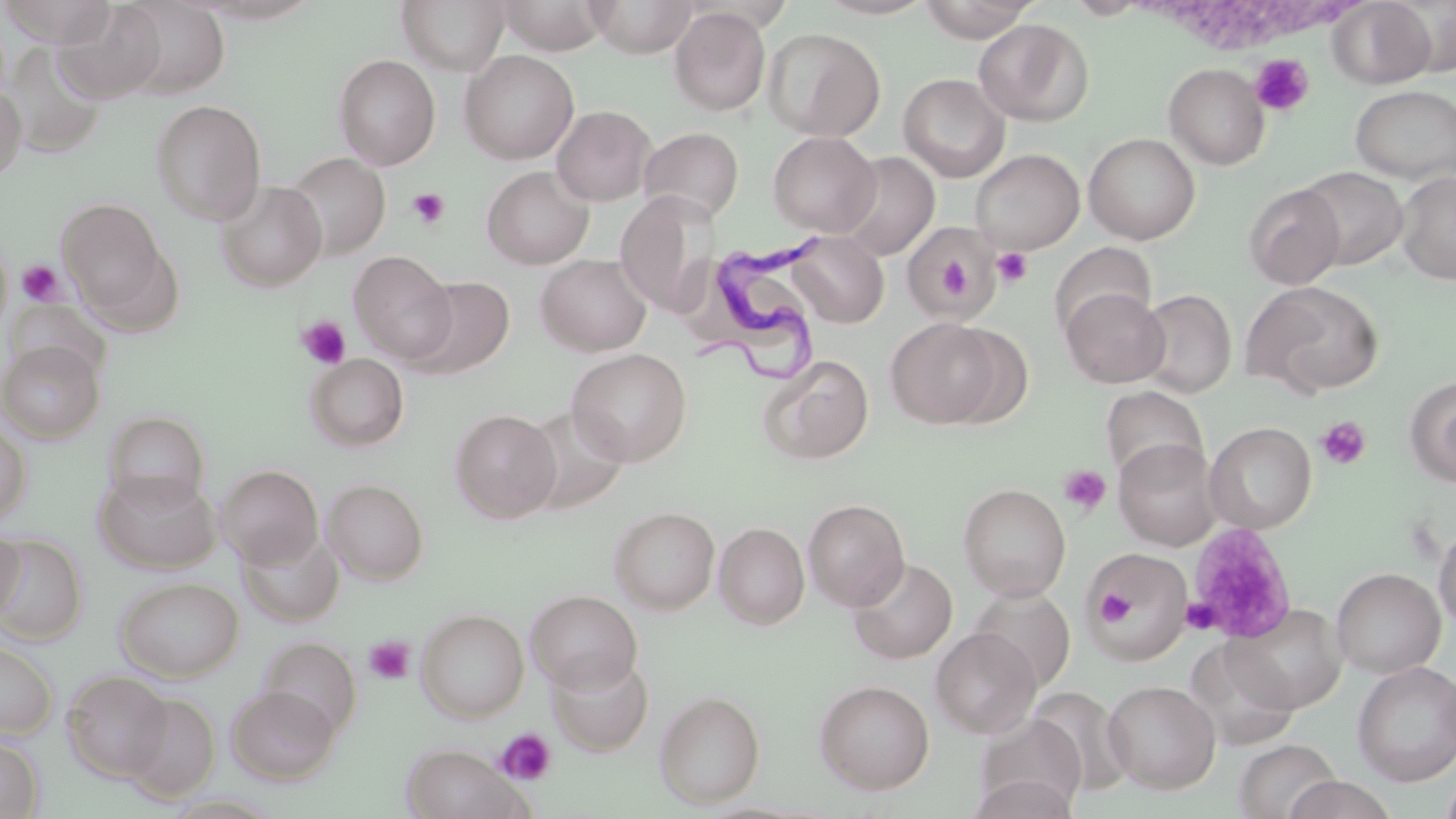 Approximate bounding boxes as [x1, y1, x2, y2] in pixels. Platelet locations: [1250, 53, 1315, 117], [407, 187, 450, 229], [992, 246, 1034, 288], [16, 260, 65, 306], [297, 315, 351, 370], [1316, 417, 1372, 470], [1058, 465, 1111, 516], [1186, 522, 1296, 641], [1097, 585, 1137, 630], [1181, 597, 1221, 634], [364, 636, 415, 686], [495, 727, 557, 785]. Trypanosoma brucei locations: [702, 231, 827, 380]. Uninfected red blood cell locations: [1, 0, 116, 46], [117, 0, 229, 97], [397, 0, 510, 75], [494, 0, 610, 54], [586, 0, 700, 57], [814, 0, 937, 19], [916, 0, 1040, 42], [1328, 0, 1435, 88], [54, 2, 167, 103], [669, 7, 770, 116], [973, 18, 1094, 126], [763, 27, 885, 141], [5, 44, 106, 159], [459, 50, 579, 164], [333, 54, 441, 170], [1164, 63, 1270, 169], [898, 73, 1010, 182], [0, 82, 27, 183], [1350, 84, 1456, 183], [150, 99, 266, 224], [551, 105, 656, 206], [637, 127, 744, 224], [768, 131, 881, 236], [1083, 133, 1200, 244], [970, 148, 1084, 253], [836, 151, 940, 260], [284, 152, 390, 258], [482, 165, 594, 269], [1297, 167, 1407, 269], [1396, 171, 1456, 284], [216, 181, 327, 291], [1244, 182, 1345, 289], [621, 196, 728, 320], [57, 198, 168, 313], [900, 222, 1002, 322], [787, 231, 889, 328], [1049, 242, 1157, 339], [349, 251, 457, 364], [536, 254, 652, 356], [406, 276, 514, 380], [1243, 279, 1385, 398], [1062, 288, 1169, 388], [1137, 289, 1237, 397], [6, 298, 109, 380], [885, 318, 1003, 428], [0, 341, 104, 442], [567, 348, 693, 467], [305, 353, 410, 452], [759, 353, 874, 464], [1406, 376, 1456, 488], [1101, 386, 1207, 485], [449, 408, 561, 524], [103, 410, 210, 509], [0, 419, 31, 524], [1204, 422, 1317, 533], [1114, 437, 1221, 549], [216, 464, 324, 567], [94, 469, 221, 574], [322, 478, 429, 584], [958, 482, 1071, 600], [803, 499, 909, 610], [609, 507, 720, 614], [1434, 518, 1456, 633], [714, 522, 809, 629], [0, 526, 25, 623], [238, 528, 343, 627], [0, 535, 88, 644], [1088, 548, 1192, 664], [847, 557, 957, 664], [1331, 567, 1445, 677], [114, 576, 244, 682], [969, 586, 1076, 690], [525, 589, 643, 693], [1225, 602, 1347, 712], [416, 608, 529, 722], [931, 627, 1041, 738], [259, 636, 362, 736], [0, 640, 58, 739], [546, 654, 654, 755], [1352, 661, 1456, 785], [62, 670, 173, 781], [814, 679, 934, 794], [1103, 680, 1221, 794], [227, 685, 340, 784], [1027, 687, 1133, 795], [654, 690, 766, 808], [121, 692, 220, 802], [975, 713, 1088, 815], [0, 735, 45, 818], [1233, 739, 1341, 819], [402, 745, 527, 819], [971, 773, 1076, 819], [1283, 774, 1397, 819]. Slide-level diagnosis: Trypanosoma brucei. May-Grünwald-Giemsa stain. Thin blood smear. Image is 1456×819 pixels. One field of a larger specimen. Captured at 1000x magnification. Light microscopy.